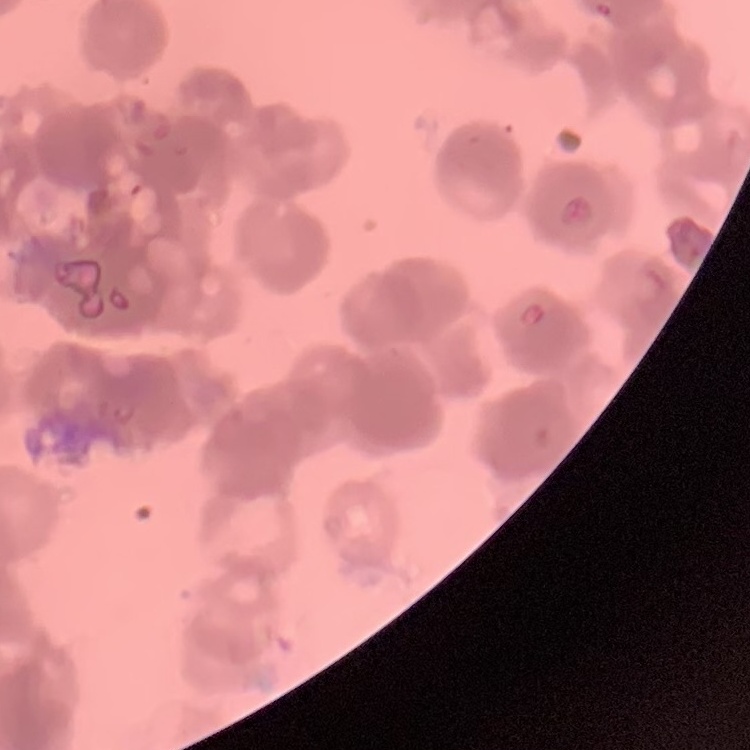
red blood cell morphology = rouleaux formation
image type = one tile cut from a larger photomicrograph
stain = Field's or Giemsa
preparation = thin blood film